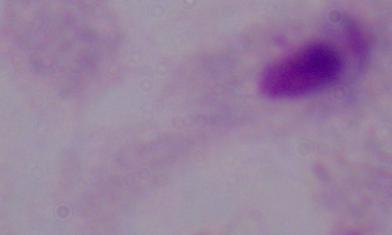
Summary:
  - Modality: micrograph
  - Identification: trichomonad
  - Magnification: 1000x